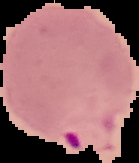

Summary:
  - Image size: 139×163 pixels
  - Image type: cell region segmented out of the field of view; surrounding area masked to black
  - Preparation: thin blood smear
  - Result: malaria parasites detected